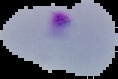 Image is 118×79 pixels. The area outside the segmented cell region is set to black. From a thin blood film. Malaria status: parasitized.